Locate every Plasmodium parasite and every leukocyte.
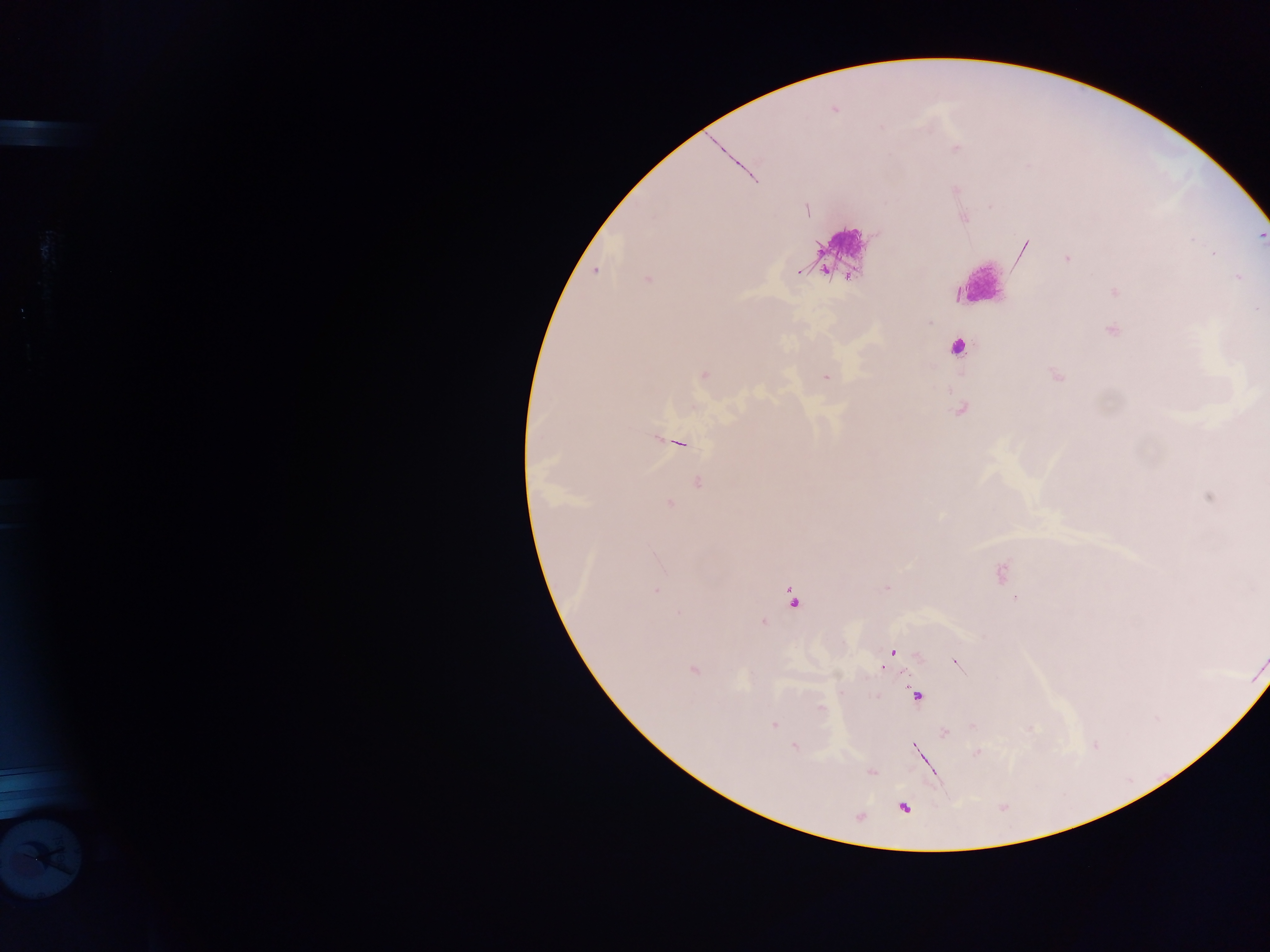

Approximate centers as x y in pixels.
Plasmodium parasites (some below the resolvable threshold): 881 128; 956 149; 955 190; 804 210; 1066 259; 797 271; 827 274; 1115 291; 1112 330; 958 347; 703 375; 1057 375; 825 376; 961 410; 659 438; 679 443; 698 482; 670 503; 999 573; 656 590; 793 599; 763 622; 887 658; 956 661; 918 697; 819 710; 774 725; 946 732; 793 746; 980 752; 870 773; 907 806.
Leukocytes: 839 243.
One object is labeled both Plasmodium parasite and leukocyte by the source: 45 862.

field of view = single
image size = 1270×952 pixels
country = Ghana
preparation = thick blood film
capture = mobile-phone photograph through a microscope